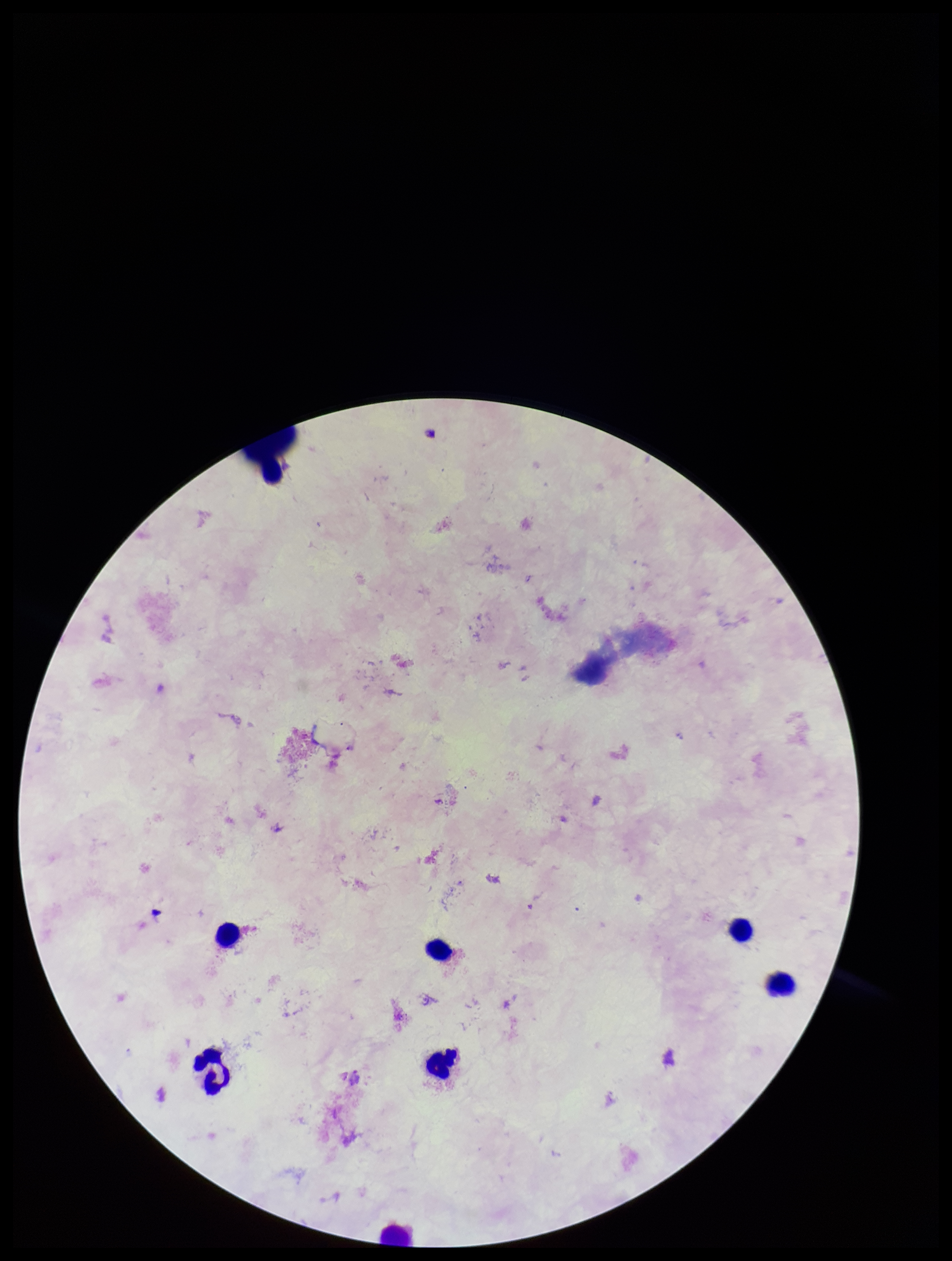 Preparation: thick. Parasite count: 0. Single field of view. Stained with Giemsa. Plasmodium parasites: none detected. Smartphone photograph taken through the eyepiece of a microscope. Patient malaria status: negative. Image is 952×1261 pixels. Leukocyte count: 7.